Point out every Plasmodium parasite.
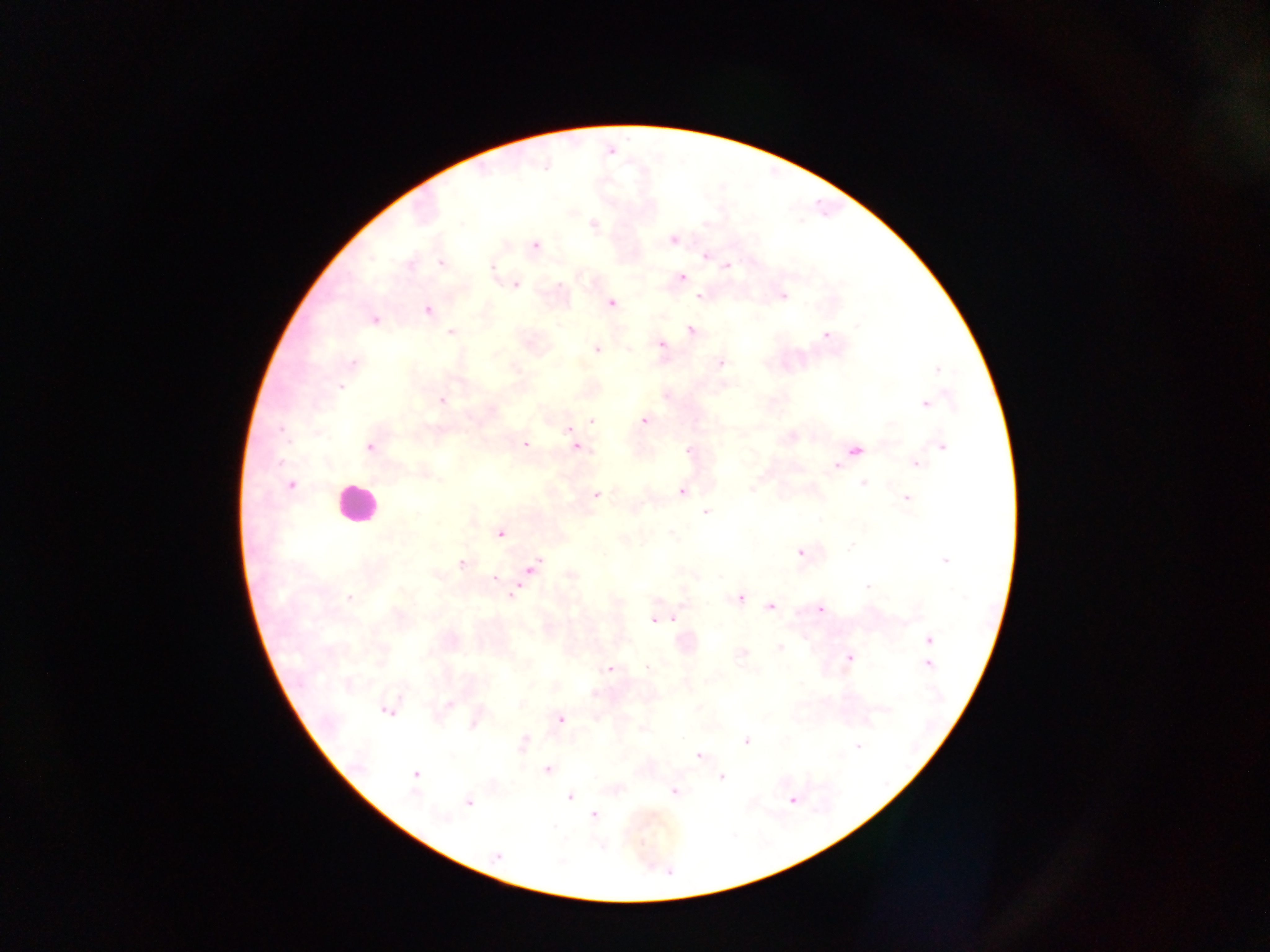

Approximate centers as (x, y) in pixels.
Plasmodium parasites: (593, 224), (673, 239), (536, 245), (706, 256), (441, 262), (410, 264), (728, 266), (492, 267), (682, 278), (516, 285), (699, 296), (784, 296), (611, 303), (427, 311), (374, 320), (858, 326), (691, 330), (451, 333), (826, 336), (660, 344), (596, 350), (354, 363), (721, 363), (937, 370), (341, 387), (441, 400), (926, 404), (592, 420), (644, 420), (281, 430), (569, 430), (525, 445), (370, 447), (577, 447), (942, 447), (688, 450), (856, 450), (916, 464), (836, 465), (863, 482), (291, 484), (750, 490), (681, 491), (597, 495), (907, 498), (705, 512), (500, 533), (850, 547), (800, 553), (945, 560), (461, 563), (532, 567), (571, 575), (720, 577), (494, 579), (867, 587), (511, 595), (348, 597), (740, 598), (771, 606), (820, 609), (673, 619), (653, 621), (929, 640), (779, 648), (743, 653), (849, 658), (928, 665), (648, 668), (609, 669), (448, 705), (388, 711), (561, 719), (473, 724), (524, 741), (746, 741), (857, 746), (698, 756), (547, 770), (416, 775), (721, 777), (674, 792), (569, 797), (791, 800), (469, 801), (593, 815), (444, 819), (498, 856).

Leukocyte locations: (353, 504). Thick blood smear. Mobile-phone photograph taken through the microscope. Image is 1270×952 pixels. One field of view. Sample from Ghana.